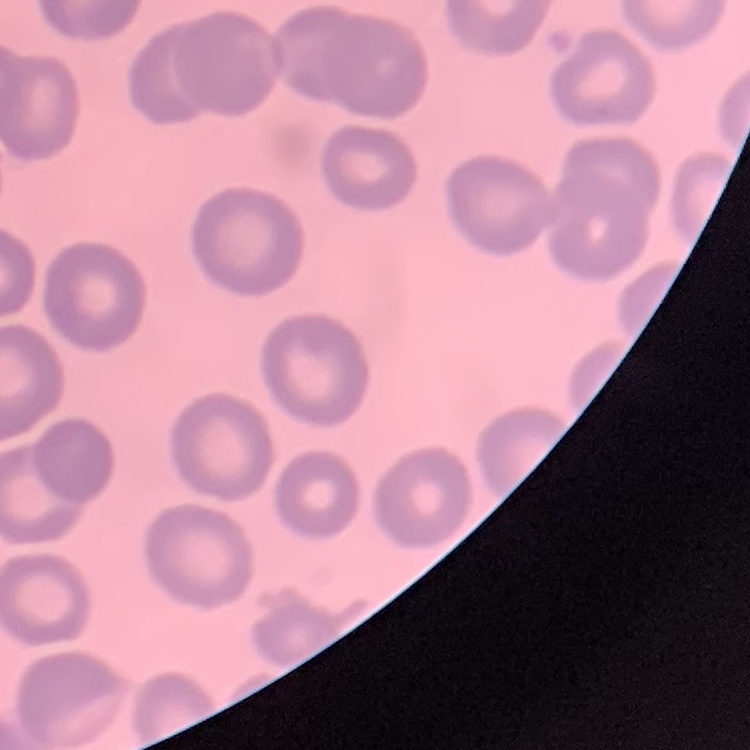

Summary:
  - Erythrocyte morphology: no rouleaux formation
  - Image type: one tile cut from a larger photomicrograph
  - Stain: Field's or Giemsa
  - Preparation: thin blood film